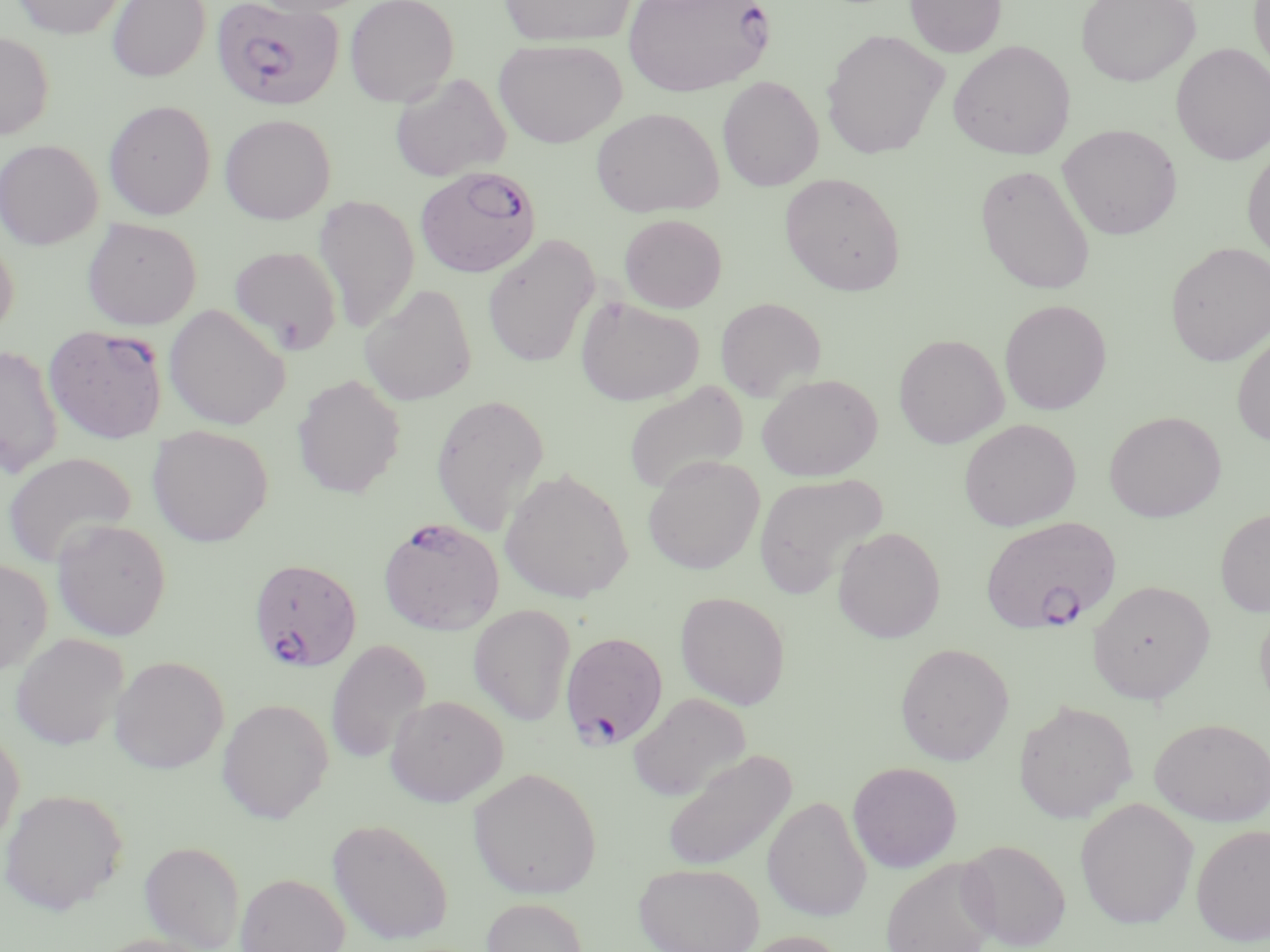

slide-level diagnosis = Plasmodium falciparum
preparation = thin blood film
uninfected red blood cell locations = approximate bounding boxes as (x1, y1, x2, y2) in pixels: (12, 0, 125, 38), (106, 0, 210, 82), (247, 0, 372, 16), (344, 0, 459, 106), (498, 0, 637, 47), (904, 0, 1007, 58), (1076, 0, 1201, 86), (1249, 0, 1270, 81), (821, 29, 949, 159), (0, 31, 54, 140), (493, 38, 627, 147), (948, 40, 1075, 160), (1171, 43, 1269, 165), (390, 73, 511, 182), (717, 76, 824, 192), (104, 100, 216, 220), (590, 106, 725, 218), (219, 113, 336, 225), (1057, 124, 1182, 240), (0, 139, 104, 250), (1243, 146, 1270, 264), (974, 163, 1096, 295), (779, 172, 906, 296), (312, 194, 420, 333), (619, 213, 727, 313), (81, 218, 202, 330), (0, 229, 19, 340), (482, 234, 600, 369), (1165, 242, 1270, 367), (229, 245, 342, 354), (359, 284, 478, 406), (575, 295, 704, 406), (715, 297, 826, 402), (999, 299, 1112, 415), (163, 304, 290, 430), (1232, 332, 1270, 446), (893, 333, 1009, 448), (0, 344, 64, 479), (757, 373, 883, 481), (292, 374, 406, 498), (623, 381, 749, 496), (430, 393, 550, 536), (1104, 410, 1226, 522), (959, 418, 1081, 531), (147, 425, 274, 547), (2, 451, 137, 569), (643, 456, 765, 575), (499, 468, 634, 603), (753, 472, 889, 599), (1215, 507, 1270, 617), (52, 519, 171, 640), (833, 527, 945, 643), (0, 558, 53, 676), (1088, 580, 1215, 704), (675, 592, 790, 709), (1255, 603, 1270, 718), (469, 604, 575, 725), (11, 633, 129, 750), (325, 637, 432, 765), (894, 642, 1014, 765), (110, 655, 229, 773), (628, 692, 751, 801), (385, 694, 508, 807), (216, 698, 334, 823), (1013, 701, 1137, 824), (1150, 717, 1270, 826), (0, 725, 25, 852), (662, 750, 796, 871), (847, 761, 963, 872), (468, 767, 602, 900), (0, 788, 128, 915), (763, 795, 872, 921), (1075, 797, 1198, 929), (327, 818, 453, 946), (1191, 824, 1270, 946), (958, 838, 1072, 951), (139, 840, 245, 951), (881, 858, 999, 952), (633, 862, 764, 952), (234, 872, 350, 952), (481, 897, 588, 951), (739, 931, 849, 952), (87, 933, 218, 952)
magnification = 1000x
image size = 1270×952 pixels
field of view = single
stain = May-Grünwald-Giemsa
modality = optical microscopy
Plasmodium falciparum-infected red blood cell locations = approximate bounding boxes as (x1, y1, x2, y2) in pixels: (212, 0, 345, 111), (622, 0, 775, 97), (415, 166, 542, 278), (44, 324, 168, 444), (979, 515, 1122, 635), (378, 516, 505, 635), (248, 557, 362, 672), (560, 631, 668, 749)